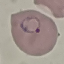

result = malaria parasites identified
image type = automatically extracted cell patch, resized to 64 × 64 pixels
capture = smartphone camera at the microscope eyepiece
preparation = thin blood smear
stain = Giemsa